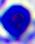
Summary:
  - Modality: micrograph
  - Magnification: 400x
  - Identification: leukocyte